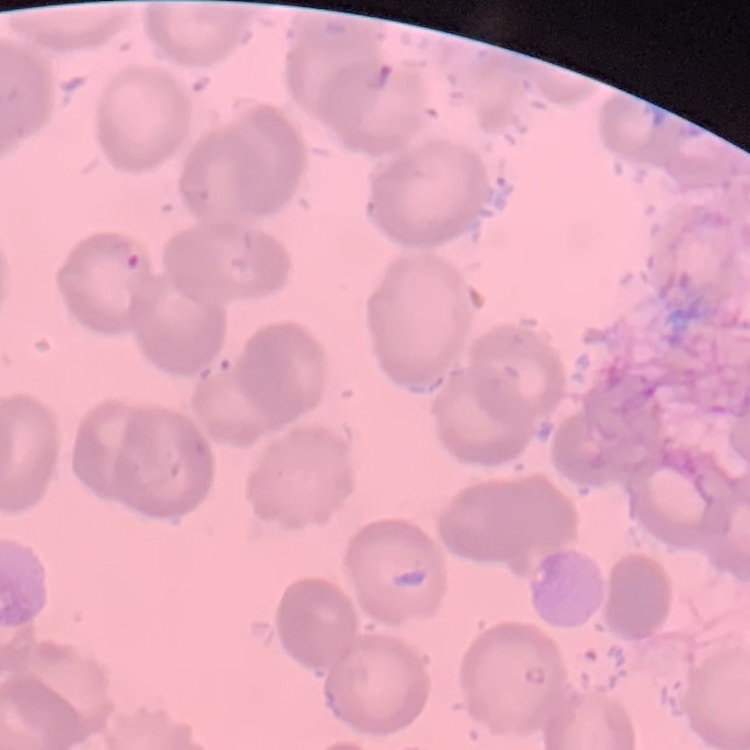

The red blood cells exhibit no rouleaux formation. Square crop of a larger photomicrograph. Thin blood smear. Field's or Giemsa stain.